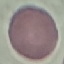

malaria status = uninfected
preparation = thin smear
stain = Giemsa
image type = automatically extracted cell patch, resized to 64 × 64 pixels
capture = smartphone camera at the microscope eyepiece